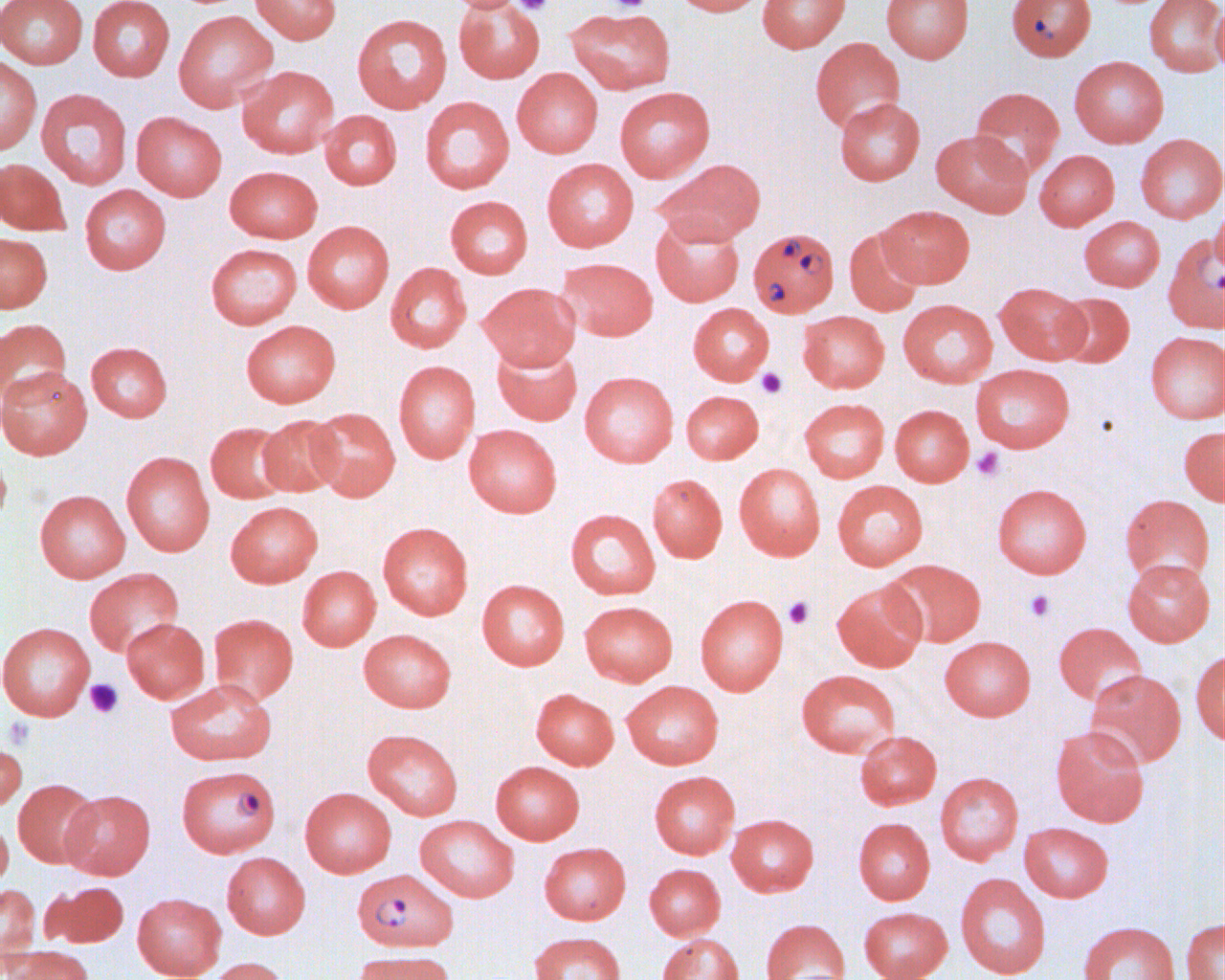
Approximate bounding boxes as named x1/y1/x2/y2 corners in pixels. Uninfected red blood cell locations: (x1=0, y1=0, x2=88, y2=68), (x1=88, y1=0, x2=175, y2=82), (x1=249, y1=0, x2=342, y2=44), (x1=443, y1=0, x2=527, y2=13), (x1=671, y1=0, x2=765, y2=16), (x1=757, y1=0, x2=851, y2=52), (x1=881, y1=0, x2=974, y2=63), (x1=1144, y1=0, x2=1225, y2=77), (x1=454, y1=1, x2=545, y2=84), (x1=1212, y1=1, x2=1225, y2=76), (x1=566, y1=6, x2=676, y2=94), (x1=173, y1=10, x2=278, y2=112), (x1=352, y1=14, x2=452, y2=113), (x1=810, y1=38, x2=905, y2=134), (x1=0, y1=55, x2=42, y2=156), (x1=1069, y1=56, x2=1169, y2=147), (x1=237, y1=65, x2=339, y2=158), (x1=512, y1=68, x2=603, y2=158), (x1=614, y1=86, x2=715, y2=182), (x1=969, y1=86, x2=1065, y2=180), (x1=36, y1=88, x2=132, y2=189), (x1=420, y1=96, x2=515, y2=193), (x1=833, y1=97, x2=925, y2=185), (x1=319, y1=110, x2=402, y2=190), (x1=131, y1=111, x2=227, y2=201), (x1=931, y1=129, x2=1033, y2=217), (x1=1135, y1=134, x2=1225, y2=223), (x1=1034, y1=149, x2=1119, y2=230), (x1=0, y1=158, x2=70, y2=236), (x1=542, y1=158, x2=639, y2=252), (x1=654, y1=158, x2=766, y2=246), (x1=225, y1=165, x2=323, y2=242), (x1=80, y1=184, x2=171, y2=275), (x1=445, y1=195, x2=533, y2=278), (x1=1212, y1=196, x2=1225, y2=278), (x1=877, y1=205, x2=974, y2=288), (x1=651, y1=216, x2=744, y2=306), (x1=1079, y1=216, x2=1165, y2=291), (x1=302, y1=221, x2=394, y2=313), (x1=844, y1=226, x2=925, y2=317), (x1=0, y1=232, x2=52, y2=313), (x1=1163, y1=233, x2=1225, y2=334), (x1=206, y1=243, x2=301, y2=329), (x1=557, y1=257, x2=658, y2=341), (x1=385, y1=262, x2=472, y2=353), (x1=478, y1=282, x2=580, y2=371), (x1=995, y1=282, x2=1090, y2=364), (x1=1054, y1=292, x2=1135, y2=368), (x1=898, y1=299, x2=998, y2=387), (x1=688, y1=303, x2=774, y2=385), (x1=798, y1=311, x2=889, y2=393), (x1=0, y1=319, x2=71, y2=406), (x1=240, y1=320, x2=341, y2=408), (x1=1145, y1=331, x2=1225, y2=423), (x1=492, y1=340, x2=582, y2=426), (x1=86, y1=342, x2=172, y2=421), (x1=393, y1=360, x2=480, y2=463), (x1=970, y1=364, x2=1074, y2=453), (x1=0, y1=366, x2=92, y2=460), (x1=579, y1=371, x2=678, y2=467), (x1=681, y1=390, x2=764, y2=464), (x1=799, y1=398, x2=890, y2=482), (x1=890, y1=405, x2=973, y2=486), (x1=306, y1=407, x2=400, y2=501), (x1=257, y1=414, x2=344, y2=497), (x1=205, y1=421, x2=293, y2=504), (x1=464, y1=424, x2=562, y2=518), (x1=1179, y1=425, x2=1225, y2=505), (x1=0, y1=445, x2=11, y2=531), (x1=121, y1=451, x2=214, y2=556), (x1=734, y1=463, x2=826, y2=560), (x1=647, y1=474, x2=727, y2=562), (x1=832, y1=479, x2=928, y2=570), (x1=992, y1=483, x2=1092, y2=578), (x1=34, y1=489, x2=131, y2=583), (x1=1120, y1=494, x2=1215, y2=586), (x1=225, y1=501, x2=323, y2=588), (x1=565, y1=509, x2=660, y2=599), (x1=377, y1=522, x2=474, y2=620), (x1=882, y1=558, x2=986, y2=647), (x1=1123, y1=558, x2=1214, y2=646), (x1=297, y1=565, x2=381, y2=651), (x1=84, y1=567, x2=184, y2=657), (x1=477, y1=579, x2=569, y2=669), (x1=831, y1=580, x2=928, y2=672), (x1=695, y1=594, x2=788, y2=694), (x1=579, y1=600, x2=678, y2=686), (x1=209, y1=613, x2=298, y2=705), (x1=121, y1=618, x2=210, y2=703), (x1=0, y1=621, x2=95, y2=720), (x1=1054, y1=622, x2=1147, y2=705), (x1=358, y1=629, x2=456, y2=712), (x1=940, y1=636, x2=1036, y2=721), (x1=1191, y1=650, x2=1225, y2=747), (x1=796, y1=669, x2=901, y2=757), (x1=1084, y1=669, x2=1186, y2=768), (x1=165, y1=678, x2=277, y2=765), (x1=621, y1=680, x2=724, y2=769), (x1=531, y1=688, x2=619, y2=770), (x1=1050, y1=724, x2=1150, y2=827), (x1=362, y1=729, x2=463, y2=820), (x1=855, y1=730, x2=942, y2=810), (x1=0, y1=740, x2=27, y2=811), (x1=490, y1=761, x2=585, y2=844), (x1=649, y1=770, x2=740, y2=859), (x1=935, y1=772, x2=1024, y2=864), (x1=13, y1=778, x2=99, y2=868), (x1=300, y1=787, x2=396, y2=877), (x1=61, y1=789, x2=155, y2=879), (x1=726, y1=813, x2=819, y2=897), (x1=415, y1=814, x2=519, y2=902), (x1=0, y1=817, x2=13, y2=889), (x1=853, y1=817, x2=935, y2=905), (x1=1019, y1=822, x2=1113, y2=902), (x1=539, y1=842, x2=631, y2=925), (x1=221, y1=852, x2=310, y2=939), (x1=644, y1=864, x2=725, y2=940), (x1=955, y1=873, x2=1051, y2=979), (x1=43, y1=881, x2=128, y2=948), (x1=0, y1=883, x2=41, y2=967), (x1=132, y1=893, x2=226, y2=979), (x1=858, y1=906, x2=952, y2=980), (x1=760, y1=918, x2=850, y2=980), (x1=1181, y1=918, x2=1224, y2=980), (x1=1077, y1=921, x2=1179, y2=980), (x1=529, y1=931, x2=626, y2=980), (x1=657, y1=933, x2=744, y2=980), (x1=5, y1=946, x2=95, y2=980), (x1=353, y1=949, x2=455, y2=980), (x1=208, y1=956, x2=289, y2=980). Platelet locations: (x1=514, y1=0, x2=553, y2=15), (x1=606, y1=0, x2=651, y2=14), (x1=756, y1=367, x2=787, y2=398), (x1=972, y1=447, x2=1004, y2=481), (x1=1023, y1=589, x2=1056, y2=623), (x1=783, y1=596, x2=814, y2=629), (x1=85, y1=678, x2=123, y2=718), (x1=4, y1=716, x2=35, y2=749). Plasmodium falciparum-infected red blood cell locations: (x1=1006, y1=0, x2=1096, y2=61), (x1=748, y1=227, x2=839, y2=317), (x1=176, y1=764, x2=280, y2=858), (x1=352, y1=867, x2=458, y2=953). Slide-level diagnosis: Plasmodium falciparum. 1000x magnification. Image is 1225×980 pixels. One field of a larger specimen. Light microscopy. Thin blood film.